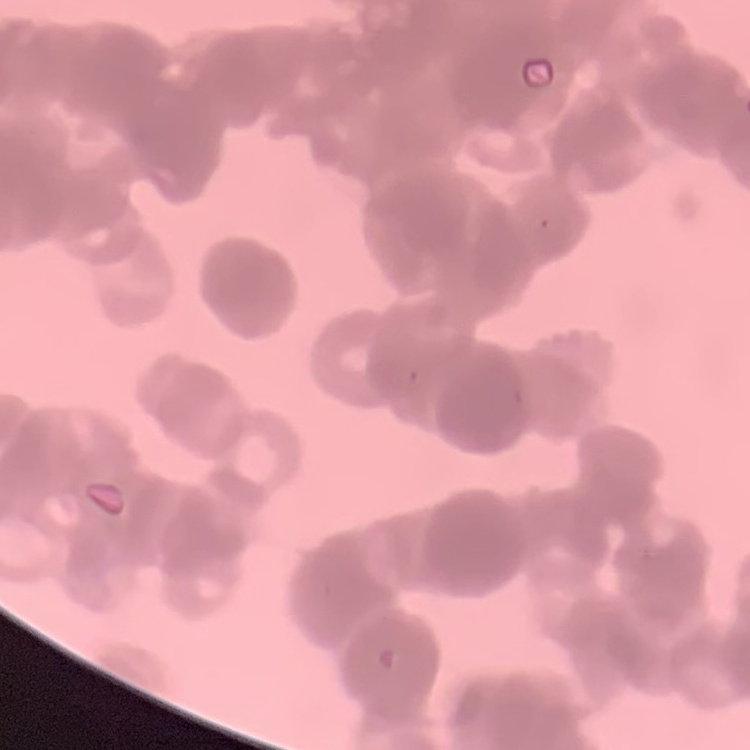

erythrocyte morphology = rouleaux formation
image type = square crop of a larger photomicrograph
stain = Field's or Giemsa
preparation = thin blood film